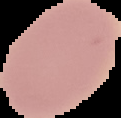 The area outside the segmented cell region is set to black. Image is 121×118 pixels. From a thin blood smear. Result: no Plasmodium parasites seen.